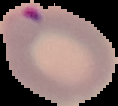
preparation = thin blood smear
image type = segmented cell region on a black background
image size = 118×106 pixels
malaria status = parasitized